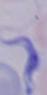

Micrograph. A trypanosome is seen. 1000x magnification.